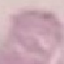

Result: no malaria parasites detected. Photographed with a smartphone camera at the microscope eyepiece. Automatically extracted cell patch, resized to 64 × 64 pixels. Thin blood smear. Giemsa-stained preparation.